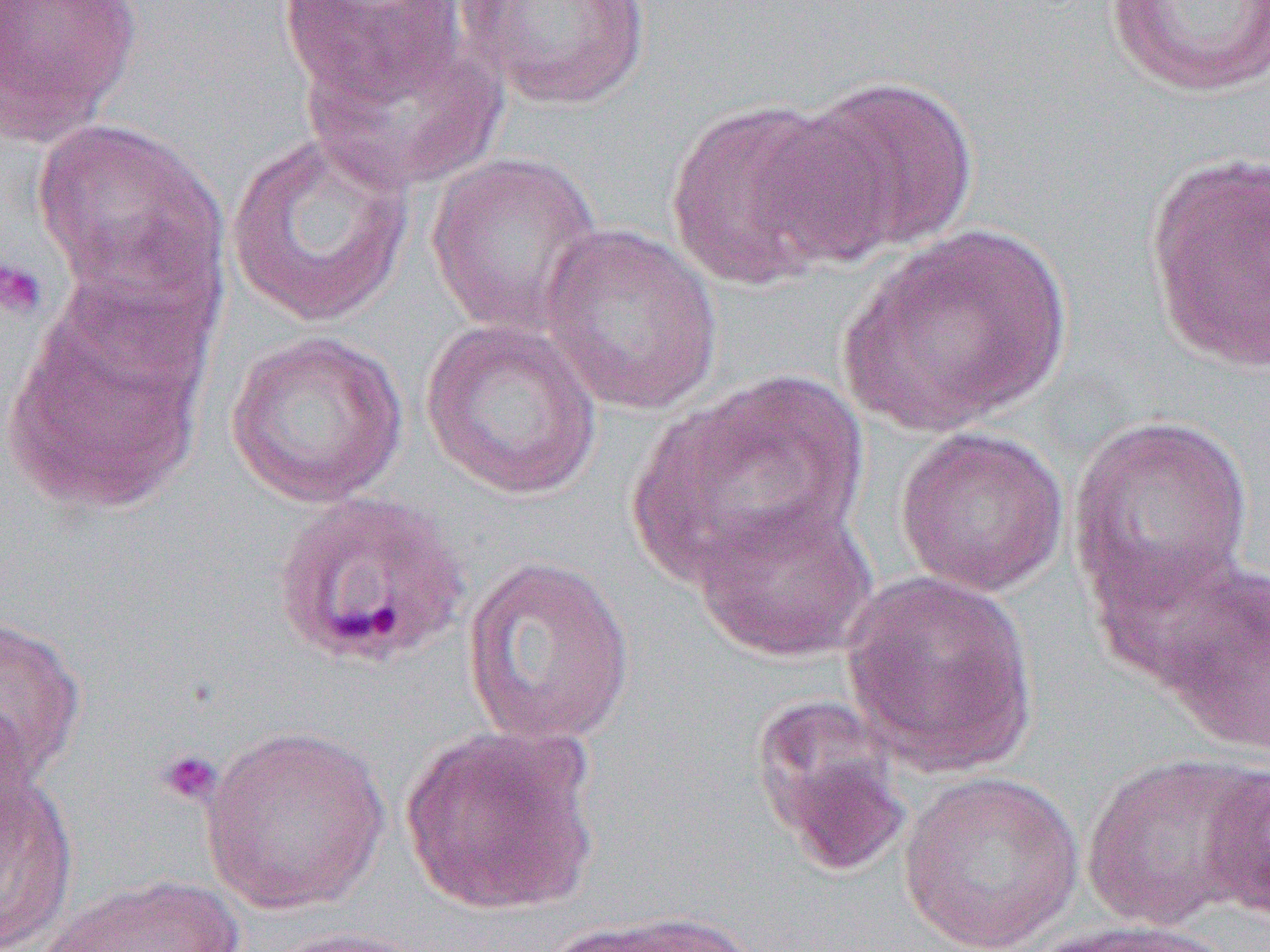
Approximate bounding boxes as [x1, y1, x2, y2] in pixels. Platelet locations: [0, 255, 48, 320], [155, 747, 224, 808]. Uninfected red blood cell locations: [0, 0, 143, 144], [456, 0, 655, 109], [277, 1, 469, 104], [1103, 1, 1270, 99], [299, 26, 507, 194], [786, 74, 982, 259], [662, 98, 860, 291], [32, 119, 229, 311], [223, 130, 419, 329], [425, 151, 606, 338], [1143, 152, 1269, 375], [536, 222, 724, 417], [842, 224, 1072, 435], [2, 293, 211, 517], [419, 317, 604, 501], [223, 330, 409, 508], [625, 371, 873, 595], [1066, 413, 1256, 612], [893, 425, 1071, 597], [691, 497, 879, 663], [1089, 540, 1264, 701], [460, 555, 636, 747], [1155, 561, 1270, 758], [840, 571, 1040, 776], [0, 614, 86, 786], [749, 694, 912, 878], [0, 698, 39, 857], [200, 724, 392, 915], [400, 724, 603, 917], [1081, 750, 1266, 931], [1200, 764, 1270, 924], [897, 770, 1086, 952], [1, 772, 78, 950], [37, 874, 247, 951], [551, 911, 757, 952], [1024, 918, 1233, 951], [254, 926, 437, 952]. Plasmodium ovale-infected red blood cell locations: [270, 488, 471, 670]. Slide-level diagnosis: Plasmodium ovale. Image is 1270×952 pixels. Captured at 1000x magnification. Light microscopy. One field of a larger specimen. Thin blood film.